State the blood parasite species.
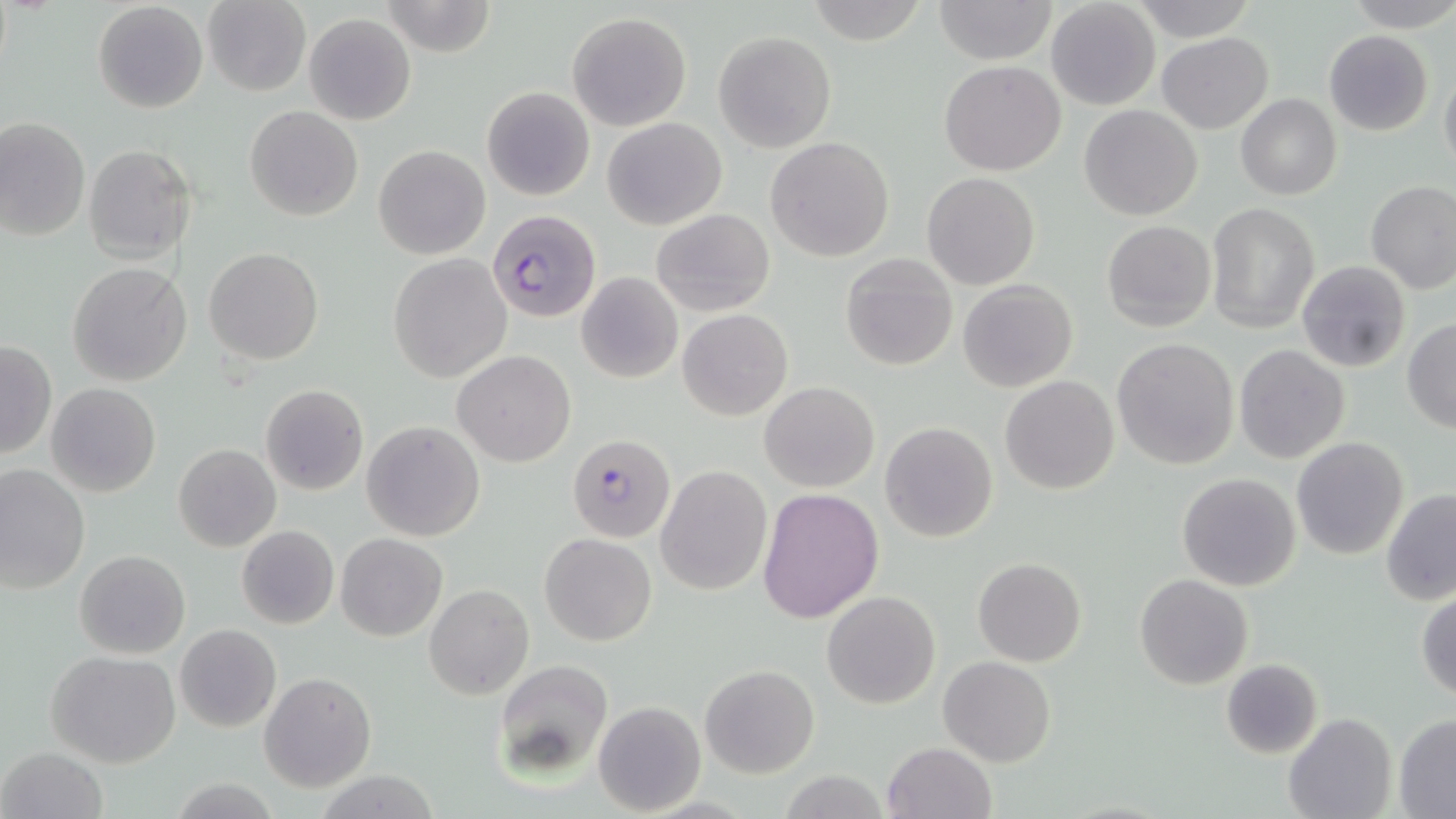

Plasmodium falciparum.

Approximate bounding boxes as (x1,y1)-(x2,y2) corner pairs in pixels. Uninfected red blood cell locations: (203,0)-(310,97), (932,0)-(1058,66), (1131,0)-(1256,40), (1345,0)-(1456,31), (380,1)-(496,57), (803,1)-(932,45), (1046,1)-(1159,111), (93,2)-(208,115), (566,12)-(691,131), (304,13)-(415,125), (1324,30)-(1433,135), (714,31)-(835,151), (1156,33)-(1273,132), (939,60)-(1066,175), (1440,62)-(1456,180), (482,86)-(595,201), (1236,94)-(1341,200), (1080,104)-(1202,220), (244,105)-(362,221), (0,117)-(90,242), (601,117)-(727,231), (765,137)-(895,261), (82,144)-(196,264), (374,145)-(491,258), (922,172)-(1039,290), (1365,180)-(1456,294), (1206,203)-(1320,333), (651,209)-(776,317), (1102,220)-(1216,331), (205,248)-(324,365), (388,253)-(512,383), (840,254)-(957,370), (1297,261)-(1411,373), (68,262)-(193,387), (576,271)-(683,384), (958,279)-(1078,392), (678,309)-(793,420), (1403,320)-(1456,433), (1112,338)-(1239,469), (1,340)-(56,460), (1233,345)-(1351,464), (453,350)-(577,467), (1001,375)-(1118,495), (759,382)-(880,493), (45,384)-(160,498), (260,384)-(369,496), (362,420)-(486,541), (880,421)-(999,543), (1292,437)-(1410,559), (173,444)-(281,552), (656,465)-(772,595), (0,466)-(90,594), (1176,473)-(1301,592), (757,488)-(883,622), (1380,488)-(1456,606), (236,525)-(338,629), (336,533)-(447,642), (539,533)-(656,645), (75,550)-(190,659), (973,557)-(1086,667), (1136,574)-(1253,690), (424,583)-(534,701), (1416,587)-(1456,703), (822,591)-(941,709), (174,624)-(281,733), (47,651)-(182,768), (939,656)-(1056,767), (493,658)-(616,778), (1220,658)-(1323,759), (700,665)-(819,778), (259,672)-(377,793), (593,700)-(706,815), (1282,712)-(1396,819), (1393,714)-(1456,815), (882,742)-(996,819), (1,746)-(110,819). Plasmodium falciparum-infected red blood cell locations: (486,211)-(601,324), (566,434)-(676,543). Image is 1456×819 pixels. Single field of view. May-Grünwald-Giemsa-stained preparation. Thin blood film. Captured at 1000x magnification. Optical microscopy.